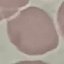
Summary:
  - Malaria status: uninfected
  - Image type: automatically extracted cell patch, resized to 64 × 64 pixels
  - Stain: Giemsa
  - Preparation: thin smear
  - Capture: smartphone through the microscope eyepiece